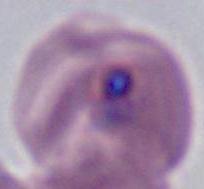

Summary:
  - Magnification: 400x or 1000x
  - Identification: Plasmodium
  - Modality: photomicrograph